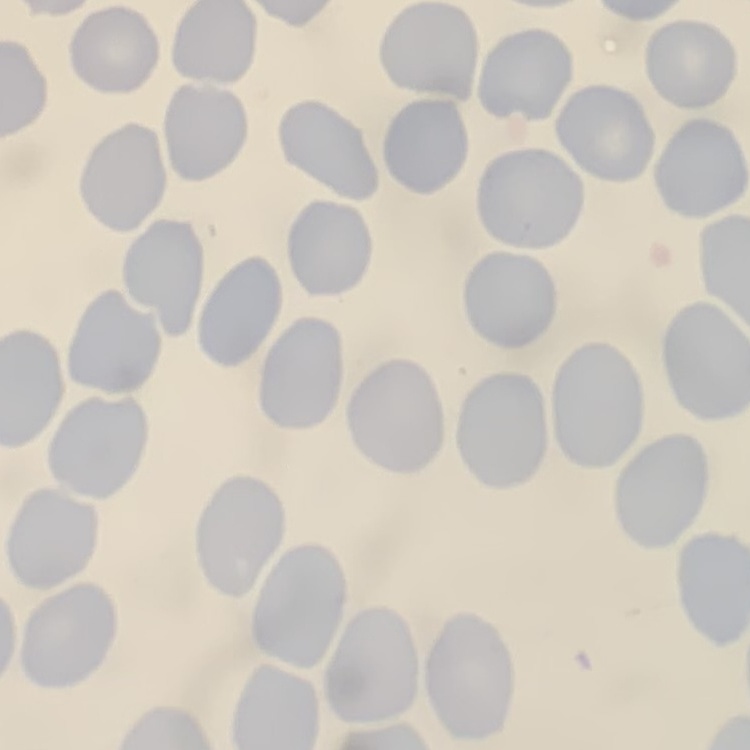

Summary:
  - Erythrocyte morphology: no rouleaux formation
  - Preparation: thin blood film
  - Stain: Field's or Giemsa
  - Image type: one tile cut from a larger photomicrograph